Classify this cell by malaria status.
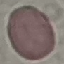

Uninfected.

Summary:
  - Capture: smartphone through the microscope eyepiece
  - Stain: Giemsa
  - Image type: automatically extracted cell patch, resized to 64 × 64 pixels
  - Preparation: thin blood smear